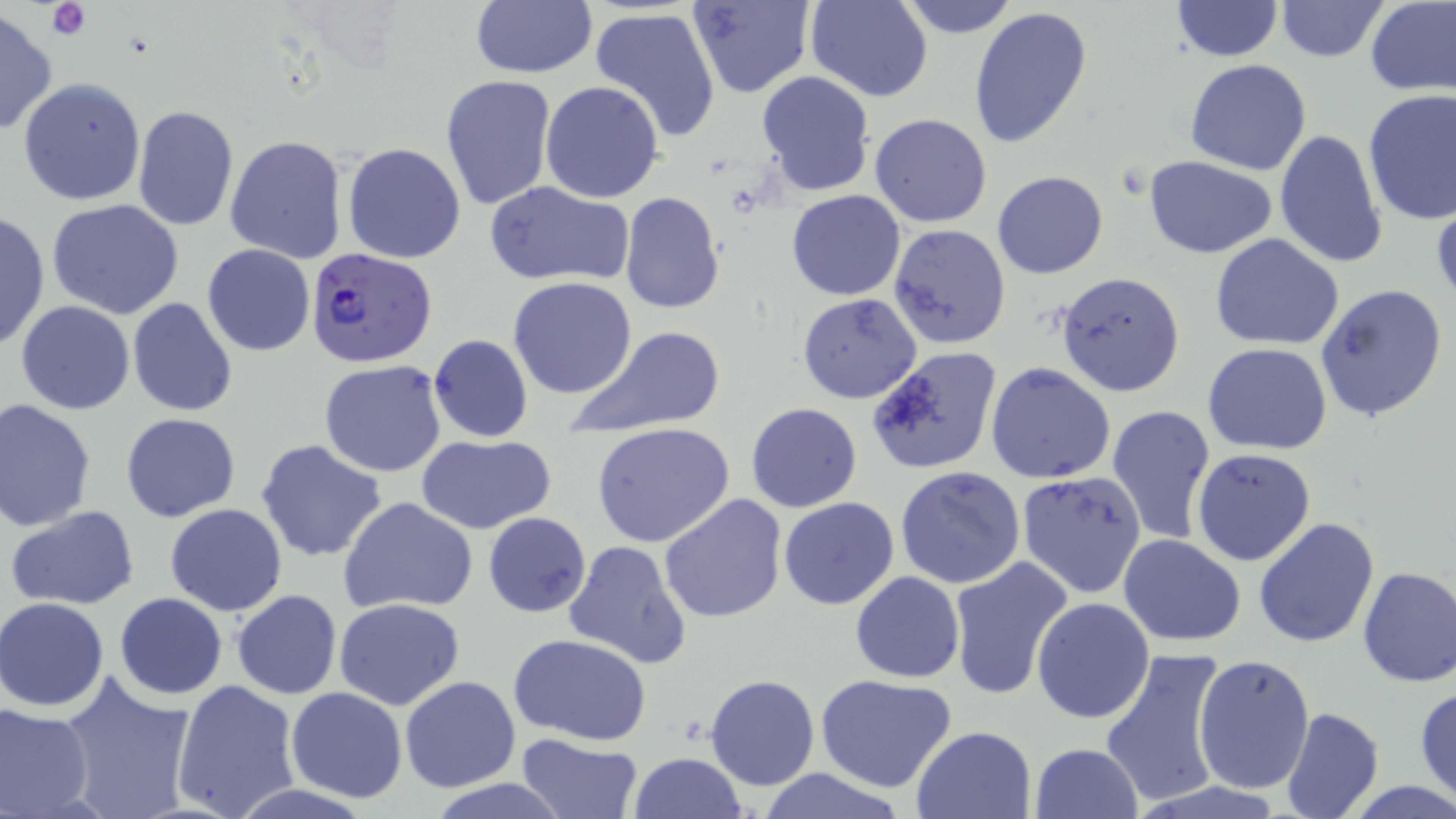
Approximate bounding boxes as (x1,y1)-(x2,y2) corner pairs in pixels. Plasmodium falciparum-infected red blood cell locations: (304,246)-(436,367). Platelet locations: (46,0)-(91,42). Uninfected red blood cell locations: (469,0)-(597,79), (688,0)-(816,100), (805,0)-(931,101), (896,0)-(1019,38), (1274,0)-(1389,62), (1364,1)-(1456,97), (1171,2)-(1282,61), (590,6)-(724,145), (968,6)-(1092,150), (0,9)-(55,138), (1185,58)-(1312,174), (756,71)-(876,197), (440,74)-(556,210), (18,77)-(145,205), (541,80)-(666,203), (1362,89)-(1456,229), (131,104)-(239,232), (870,113)-(992,228), (1274,129)-(1390,270), (225,136)-(348,263), (342,142)-(467,264), (1142,156)-(1279,256), (992,170)-(1108,278), (485,180)-(632,287), (786,190)-(906,300), (619,192)-(727,314), (47,199)-(186,318), (0,210)-(49,353), (887,223)-(1011,348), (1211,233)-(1346,350), (202,243)-(315,356), (1055,271)-(1185,395), (508,277)-(638,399), (1315,283)-(1449,423), (797,293)-(922,404), (127,298)-(237,417), (14,300)-(135,414), (565,325)-(727,438), (428,335)-(533,442), (1203,343)-(1332,454), (865,345)-(1003,474), (320,360)-(448,477), (985,362)-(1116,484), (1,398)-(98,532), (745,402)-(863,513), (1105,403)-(1216,546), (120,412)-(242,523), (591,422)-(737,548), (414,434)-(557,534), (256,438)-(388,561), (1192,448)-(1317,567), (895,466)-(1025,589), (1017,469)-(1145,599), (658,493)-(788,626), (777,496)-(899,610), (338,497)-(481,617), (165,503)-(288,616), (6,507)-(141,610), (482,512)-(592,617), (1253,517)-(1380,648), (1118,534)-(1245,646), (564,540)-(694,669), (948,556)-(1075,703), (1357,566)-(1456,689), (849,571)-(964,682), (232,590)-(343,699), (113,593)-(226,700), (1031,596)-(1156,724), (1,597)-(112,711), (334,598)-(467,711), (509,634)-(653,745), (1099,648)-(1230,809), (1192,654)-(1314,796), (58,672)-(197,819), (815,674)-(958,793), (704,675)-(819,791), (399,676)-(520,792), (171,678)-(300,819), (1415,686)-(1456,805), (285,687)-(409,802), (0,702)-(95,818), (1281,706)-(1384,819), (911,725)-(1037,817), (513,733)-(642,819), (1030,742)-(1143,818), (628,751)-(746,819), (751,767)-(912,819), (428,780)-(571,818). Slide-level diagnosis: Plasmodium falciparum. Image is 1456×819 pixels. May-Grünwald-Giemsa-stained preparation. One field of a larger specimen. Optical microscopy. Thin blood smear. Captured at 1000x magnification.